Assess this cell for malaria.
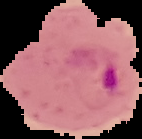
It is parasitized.

The area outside the segmented cell region is set to black. Image is 142×139 pixels. From a thin blood smear.